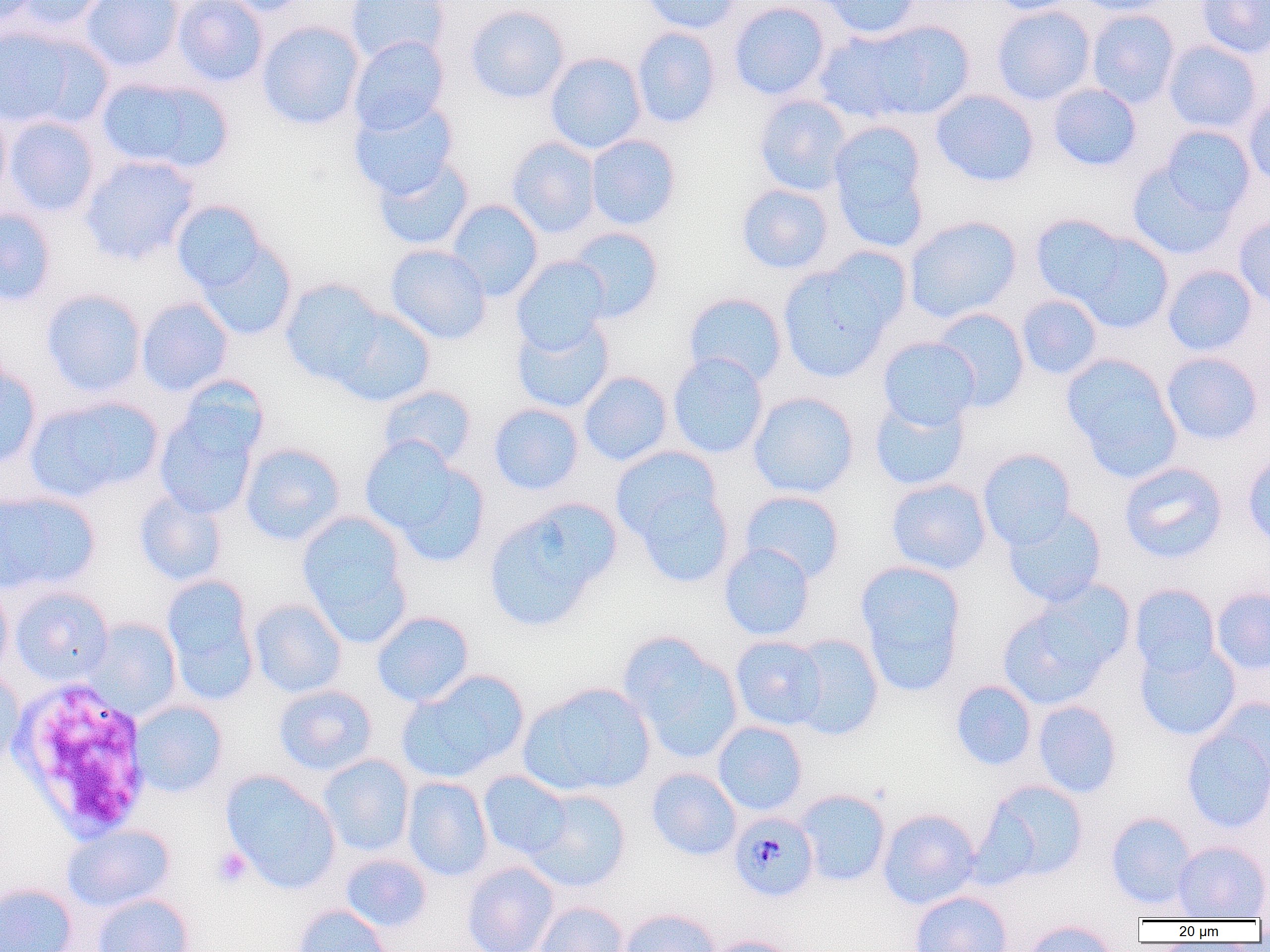

Approximate bounding boxes as (x1, y1, x2, y2) in pixels. White blood cell locations: (7, 678, 154, 842). Plasmodium malariae-infected red blood cell locations: (728, 812, 819, 902). Platelet locations: (211, 846, 253, 888). Uninfected red blood cell locations: (0, 0, 41, 27), (10, 0, 110, 32), (80, 0, 184, 73), (172, 0, 268, 87), (213, 0, 315, 16), (344, 0, 452, 64), (639, 0, 744, 34), (817, 0, 923, 39), (988, 0, 1080, 15), (1072, 0, 1176, 16), (1197, 0, 1270, 59), (728, 1, 832, 101), (464, 4, 570, 104), (991, 5, 1096, 106), (1086, 8, 1180, 108), (823, 20, 974, 123), (255, 21, 365, 130), (0, 25, 108, 131), (631, 26, 722, 129), (348, 35, 450, 135), (1163, 40, 1263, 135), (545, 52, 647, 154), (95, 76, 233, 174), (1047, 83, 1142, 171), (930, 89, 1040, 187), (753, 95, 853, 196), (1243, 95, 1270, 189), (349, 98, 459, 200), (0, 105, 12, 204), (3, 116, 102, 217), (827, 122, 931, 252), (1158, 125, 1256, 218), (580, 133, 672, 323), (586, 134, 681, 230), (507, 137, 601, 238), (79, 155, 200, 266), (372, 155, 474, 252), (1126, 160, 1239, 260), (736, 183, 834, 274), (446, 199, 544, 302), (170, 200, 270, 297), (0, 207, 57, 308), (1030, 214, 1130, 307), (904, 215, 1022, 324), (1233, 215, 1270, 310), (565, 227, 665, 324), (1070, 231, 1174, 333), (194, 238, 298, 341), (385, 244, 492, 345), (821, 247, 913, 333), (511, 256, 611, 353), (778, 261, 896, 383), (1162, 265, 1258, 357), (280, 278, 389, 388), (40, 289, 146, 397), (683, 292, 787, 388), (1016, 294, 1103, 380), (136, 297, 234, 396), (328, 306, 436, 407), (931, 308, 1030, 411), (511, 315, 615, 414), (877, 336, 981, 431), (1161, 352, 1264, 445), (667, 353, 769, 459), (1062, 354, 1182, 479), (0, 361, 43, 470), (578, 371, 672, 466), (175, 375, 269, 463), (377, 384, 477, 469), (748, 392, 859, 499), (25, 395, 163, 502), (868, 396, 970, 492), (488, 403, 584, 495), (154, 408, 260, 520), (361, 437, 488, 566), (240, 442, 346, 546), (611, 447, 723, 547), (977, 448, 1077, 550), (1242, 453, 1270, 547), (1119, 462, 1228, 563), (624, 477, 737, 588), (885, 478, 992, 576), (0, 489, 100, 595), (133, 489, 228, 587), (739, 489, 845, 583), (482, 499, 620, 632), (1003, 505, 1107, 607), (296, 510, 411, 640), (718, 543, 816, 641), (855, 560, 967, 695), (160, 576, 259, 705), (0, 580, 14, 684), (1129, 583, 1221, 678), (9, 585, 114, 686), (1211, 587, 1270, 675), (248, 598, 347, 698), (997, 600, 1114, 710), (371, 611, 474, 707), (83, 618, 182, 719), (619, 633, 743, 763), (788, 633, 884, 740), (730, 635, 827, 731), (1134, 642, 1241, 741), (398, 669, 530, 782), (0, 670, 25, 771), (950, 679, 1037, 771), (518, 682, 656, 797), (273, 685, 377, 776), (1209, 697, 1270, 792), (129, 700, 228, 798), (1032, 700, 1122, 798), (712, 721, 808, 816), (1181, 721, 1270, 834), (318, 754, 415, 857), (646, 767, 741, 861), (220, 770, 342, 894), (478, 770, 572, 861), (402, 776, 493, 881), (978, 780, 1090, 884), (523, 788, 631, 892), (795, 789, 891, 887), (877, 808, 981, 909), (1106, 811, 1197, 909), (61, 823, 176, 913), (1172, 841, 1270, 920), (339, 852, 432, 933), (462, 861, 559, 952), (0, 882, 78, 952), (1253, 883, 1270, 926), (909, 890, 1013, 952), (91, 893, 195, 952), (532, 901, 629, 952), (291, 903, 395, 952), (617, 908, 722, 952), (1021, 920, 1119, 952), (705, 936, 800, 952). Slide-level diagnosis: Plasmodium malariae. Thin blood smear. 1000x magnification. Light microscopy. Image is 1270×952 pixels. One field of a larger specimen.